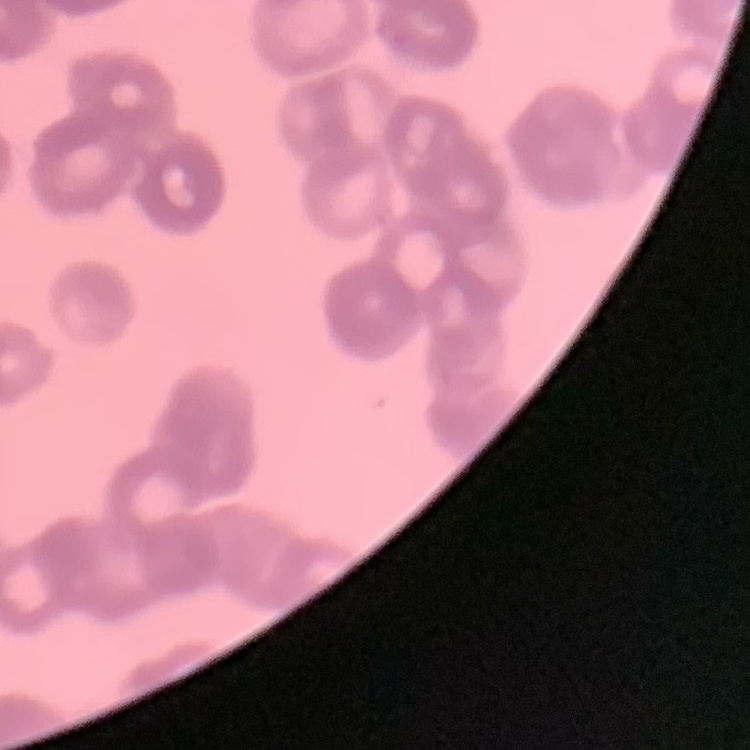

{
  "red_blood_cell_morphology": "rouleaux formation",
  "preparation": "thin blood smear",
  "stain": "Field's or Giemsa",
  "image_type": "square crop of a larger photomicrograph"
}